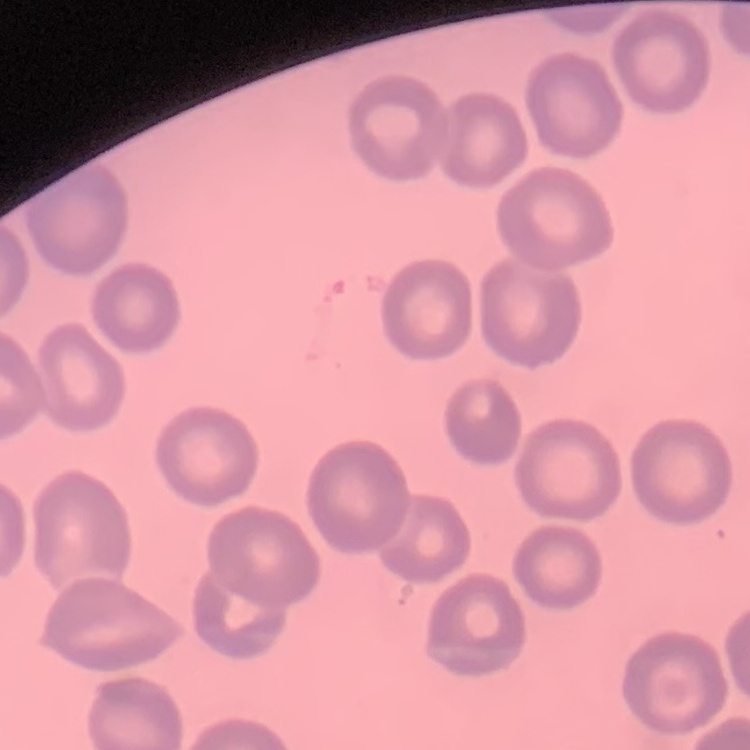

The erythrocytes show no rouleaux formation. One tile cut from a larger photomicrograph. Thin blood smear. Stained with either Field's or Giemsa.